Assess the morphology of the red blood cells.
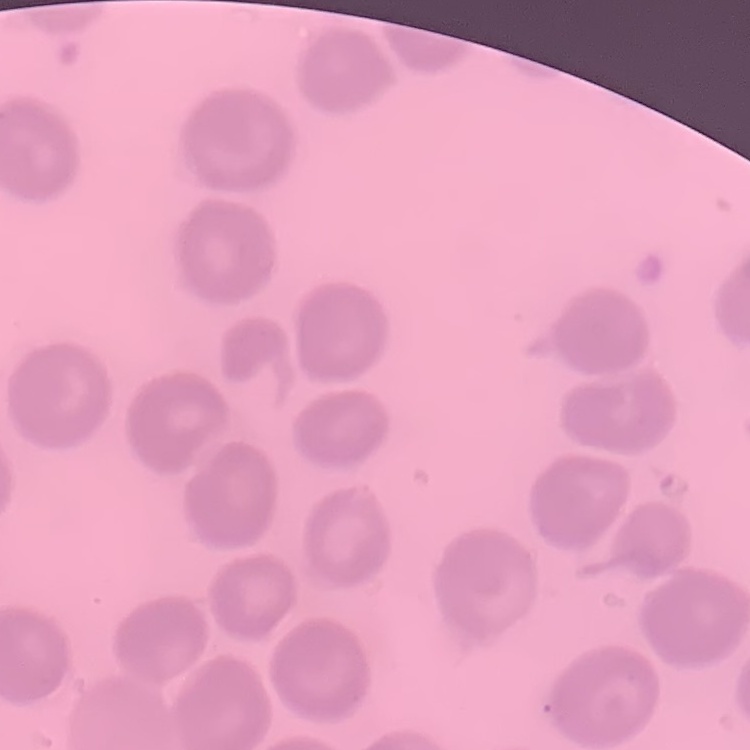
No rouleaux formation.

Summary:
  - Image type: square crop of a larger photomicrograph
  - Preparation: thin blood film
  - Stain: Field's or Giemsa